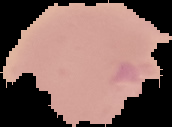 Image is 172×127 pixels. From a thin blood smear. Malaria status: uninfected. Segmented cell region on a black background.